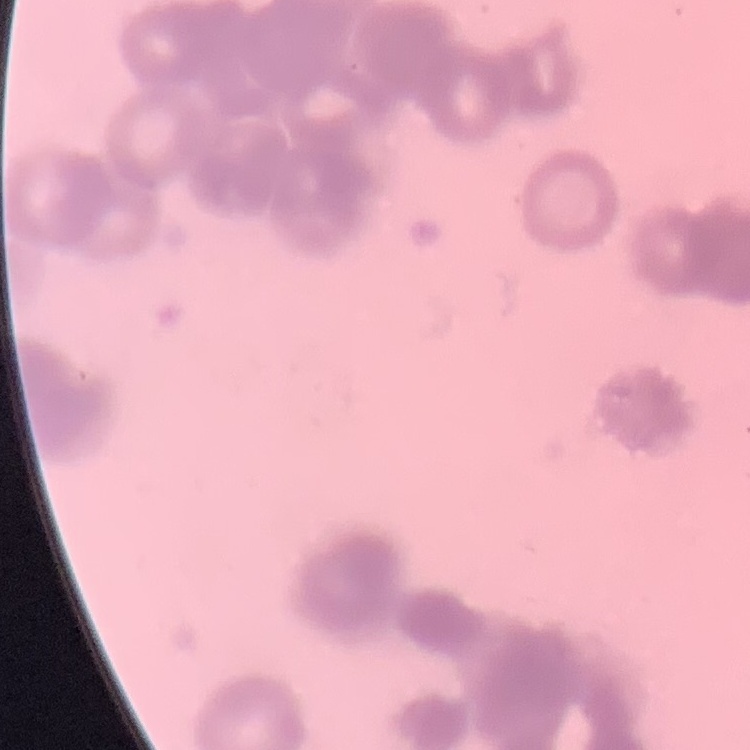

erythrocyte morphology = rouleaux formation
image type = one tile cut from a larger photomicrograph
stain = Field's or Giemsa
preparation = thin blood smear